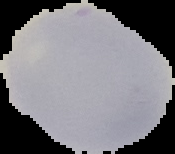
image_size: 175×154 pixels
malaria_status: uninfected
preparation: thin blood smear
image_type: cell region segmented out of the field of view; surrounding area masked to black